Identify the preparation type.
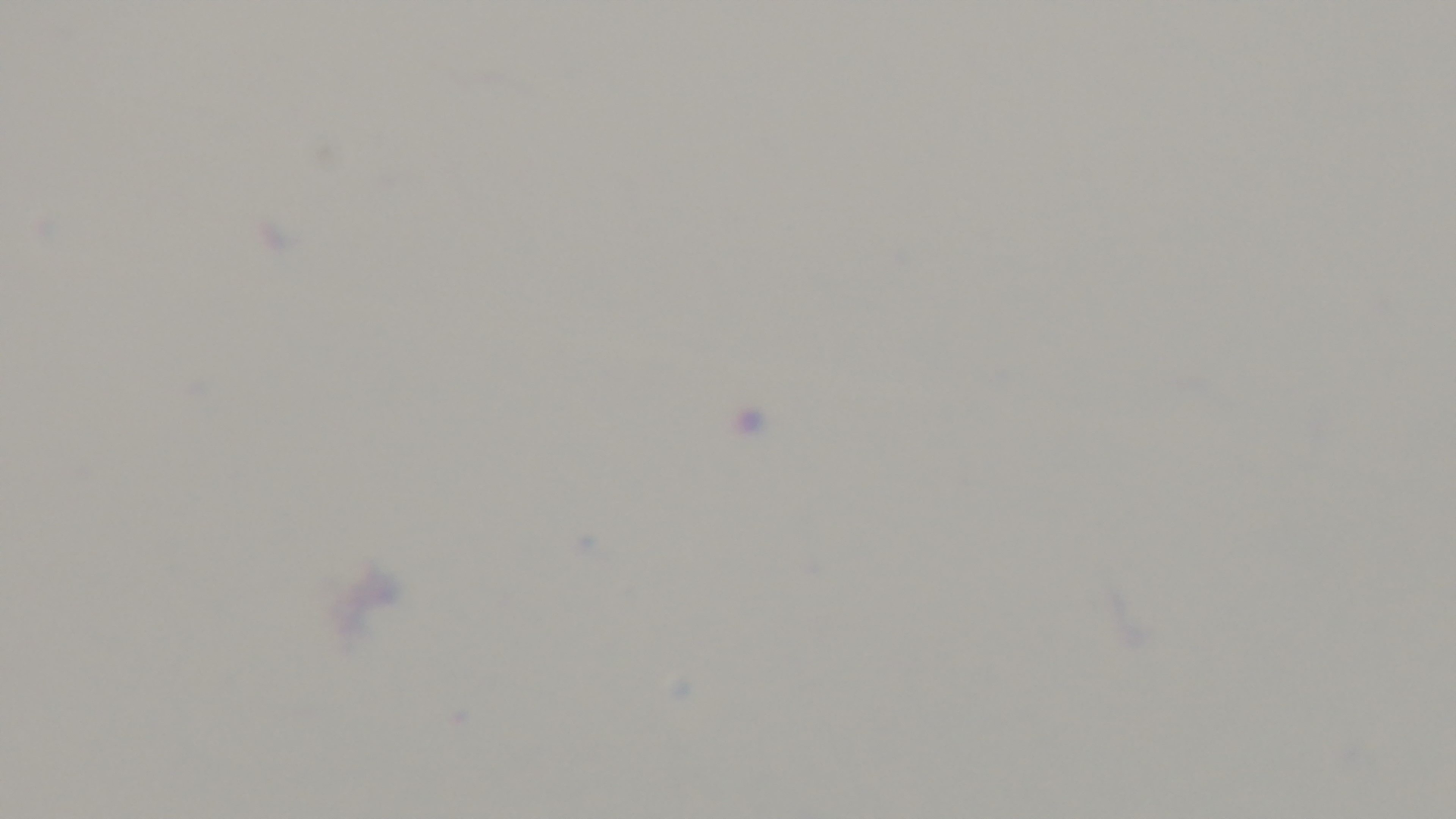
Thick.

Summary:
  - Malaria status: negative
  - Field of view: one from the slide
  - Objective: 100x oil immersion
  - Capture: mounted 4K digital camera
  - Modality: light microscopy
  - Stain: Giemsa